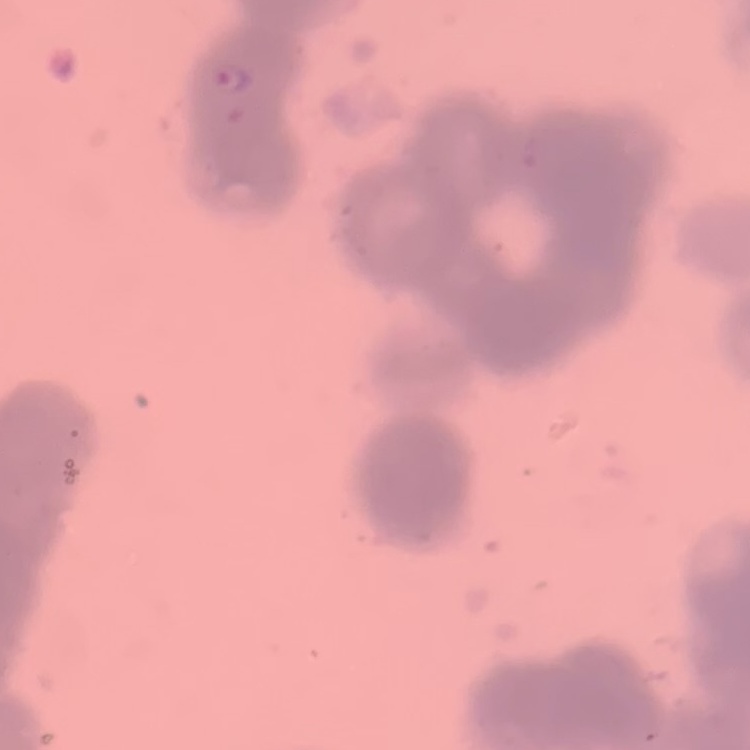
{
  "red_blood_cell_morphology": "rouleaux formation",
  "preparation": "thin peripheral smear",
  "image_type": "square crop of a larger photomicrograph",
  "stain": "Field's or Giemsa"
}